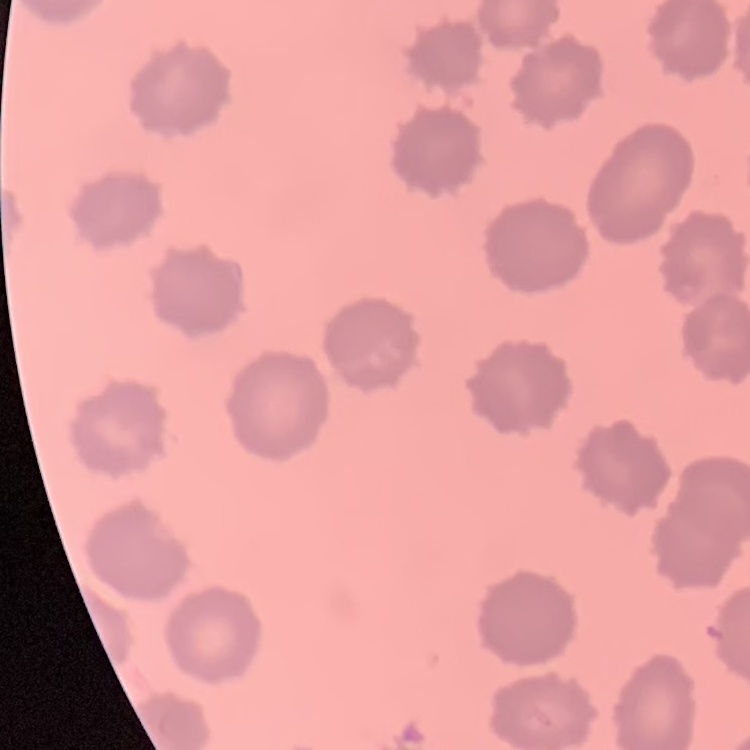
Summary:
  - Red blood cell morphology: no rouleaux formation
  - Stain: Field's or Giemsa
  - Image type: one tile cut from a larger photomicrograph
  - Preparation: thin peripheral smear